Identify the preparation type.
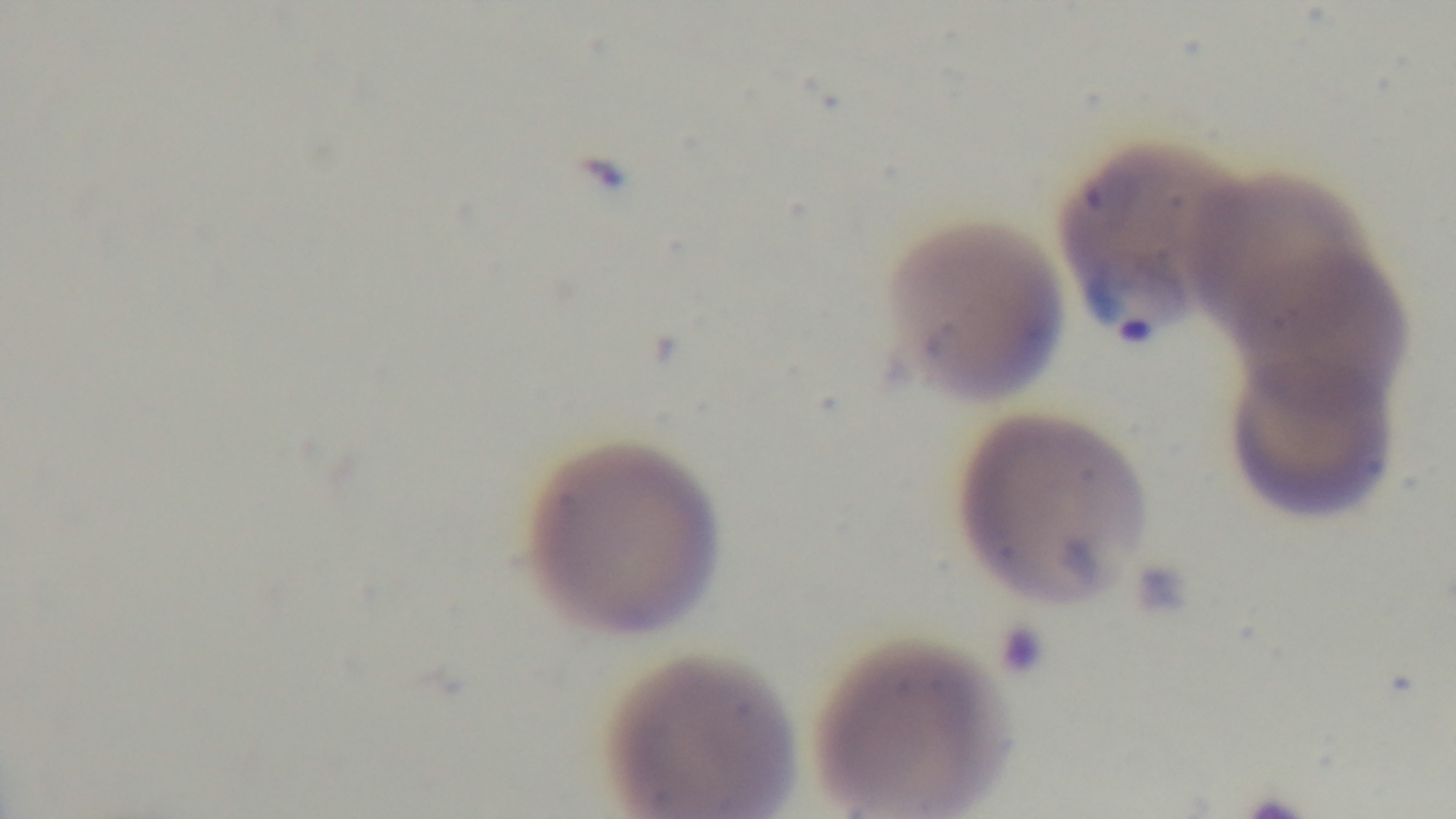

A thin smear.

Mounted 4K digital camera. Photomicrograph. Giemsa-stained. 100x oil-immersion objective. Single field of view. Malaria status: positive.